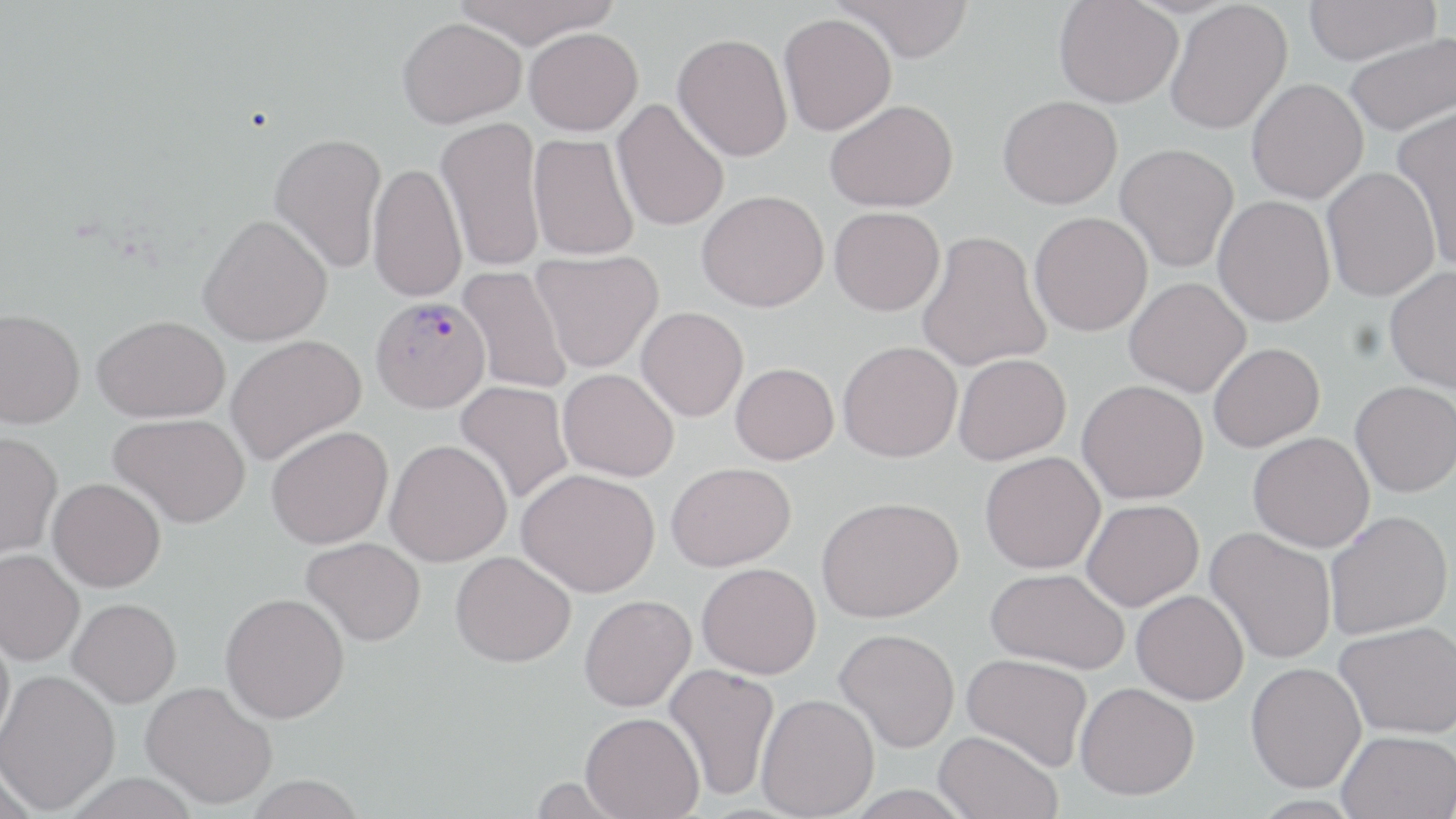
Summary:
  - Coordinate format: approximate bounding boxes as (x1, y1, x2, y2) in pixels
  - Uninfected red blood cell locations: (451, 0, 621, 49), (834, 0, 975, 62), (1054, 0, 1183, 108), (1301, 0, 1440, 65), (1165, 1, 1293, 135), (779, 13, 896, 135), (397, 17, 526, 128), (525, 27, 643, 136), (673, 32, 793, 161), (1345, 33, 1456, 137), (1246, 78, 1368, 204), (998, 95, 1122, 208), (612, 99, 730, 232), (824, 99, 958, 212), (1392, 104, 1456, 270), (436, 116, 546, 272), (269, 132, 387, 273), (528, 133, 640, 261), (1115, 143, 1239, 272), (367, 161, 466, 303), (1321, 167, 1440, 301), (697, 189, 829, 312), (1213, 195, 1335, 326), (829, 206, 945, 315), (1029, 211, 1153, 336), (198, 213, 333, 346), (917, 230, 1051, 372), (531, 249, 663, 373), (1383, 265, 1456, 393), (457, 266, 571, 395), (1124, 278, 1251, 396), (636, 307, 748, 421), (0, 308, 84, 428), (93, 314, 230, 423), (225, 334, 366, 465), (838, 340, 963, 462), (1209, 342, 1324, 452), (953, 353, 1071, 464), (731, 362, 839, 464), (558, 368, 679, 482), (1077, 379, 1208, 504), (1350, 380, 1456, 497), (455, 381, 575, 505), (109, 413, 250, 528), (266, 425, 393, 549), (0, 432, 62, 559), (1248, 432, 1374, 552), (385, 439, 512, 566), (980, 451, 1105, 573), (666, 461, 795, 571), (517, 468, 660, 597), (47, 477, 166, 592), (816, 496, 964, 623), (1081, 499, 1204, 610), (1325, 510, 1452, 639), (1206, 527, 1336, 665), (301, 536, 427, 647), (0, 549, 84, 666), (450, 551, 576, 667), (697, 562, 821, 679), (985, 567, 1130, 673), (1131, 590, 1249, 705), (220, 592, 350, 723), (579, 595, 696, 711), (68, 598, 181, 707), (1335, 620, 1456, 738), (0, 622, 15, 751), (835, 628, 960, 752), (962, 653, 1093, 771), (1245, 661, 1366, 792), (664, 663, 781, 801), (0, 670, 120, 814), (141, 680, 278, 809), (1075, 682, 1199, 800), (756, 693, 879, 818), (580, 712, 705, 819), (1337, 729, 1456, 819), (934, 730, 1063, 819), (0, 770, 38, 819), (63, 774, 202, 819), (241, 775, 369, 819)
  - Plasmodium vivax-infected red blood cell locations: (370, 295, 491, 413)
  - Slide-level diagnosis: Plasmodium vivax
  - Image size: 1456×819 pixels
  - Magnification: 1000x
  - Preparation: thin blood film
  - Stain: May-Grünwald-Giemsa
  - Field of view: one of a larger specimen
  - Modality: optical microscopy